Describe the morphology of the erythrocytes.
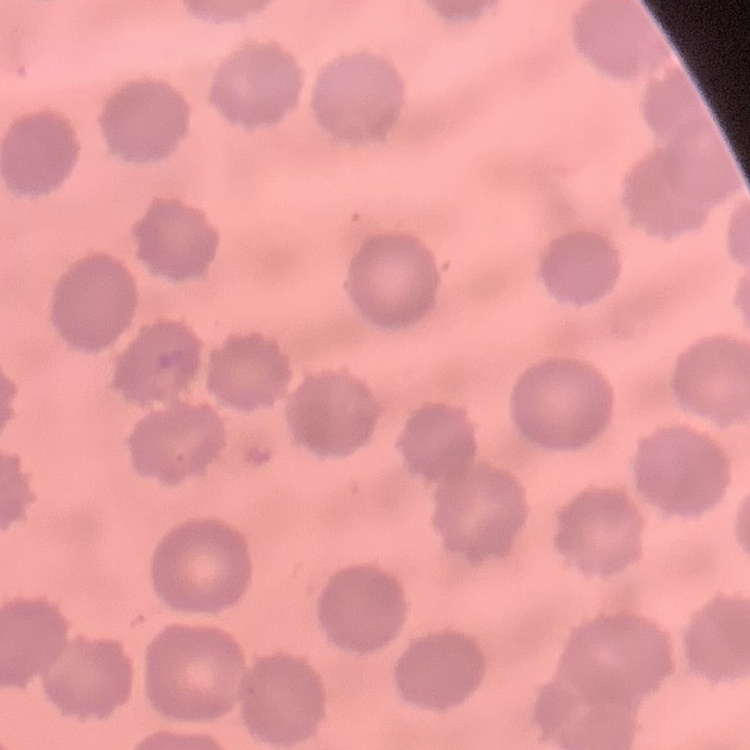
They show no rouleaux formation.

Summary:
  - Stain: Field's or Giemsa
  - Preparation: thin blood film
  - Image type: one tile cut from a larger photomicrograph